Report the malaria status.
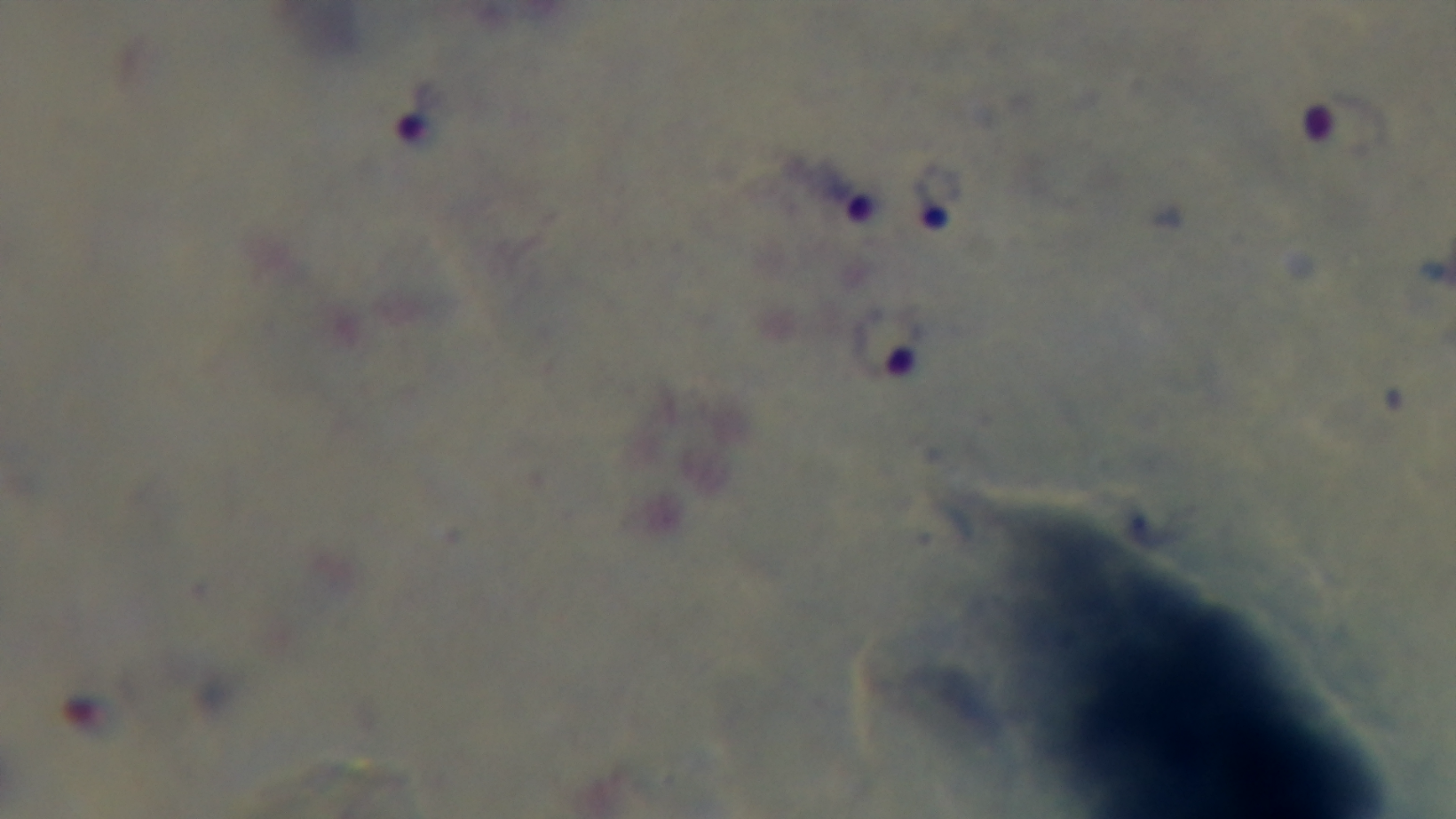
Infected.

Summary:
  - Modality: light microscopy
  - Field of view: one from the slide
  - Stain: Giemsa
  - Objective: 100x oil immersion
  - Capture: mounted 4K digital camera
  - Preparation: thick smear